Report the malaria status of this cell.
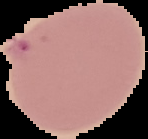
Uninfected.

Image is 148×139 pixels. From a thin blood smear. Cell region segmented out of the field of view; the surrounding area is masked to black.